Evaluate for malaria.
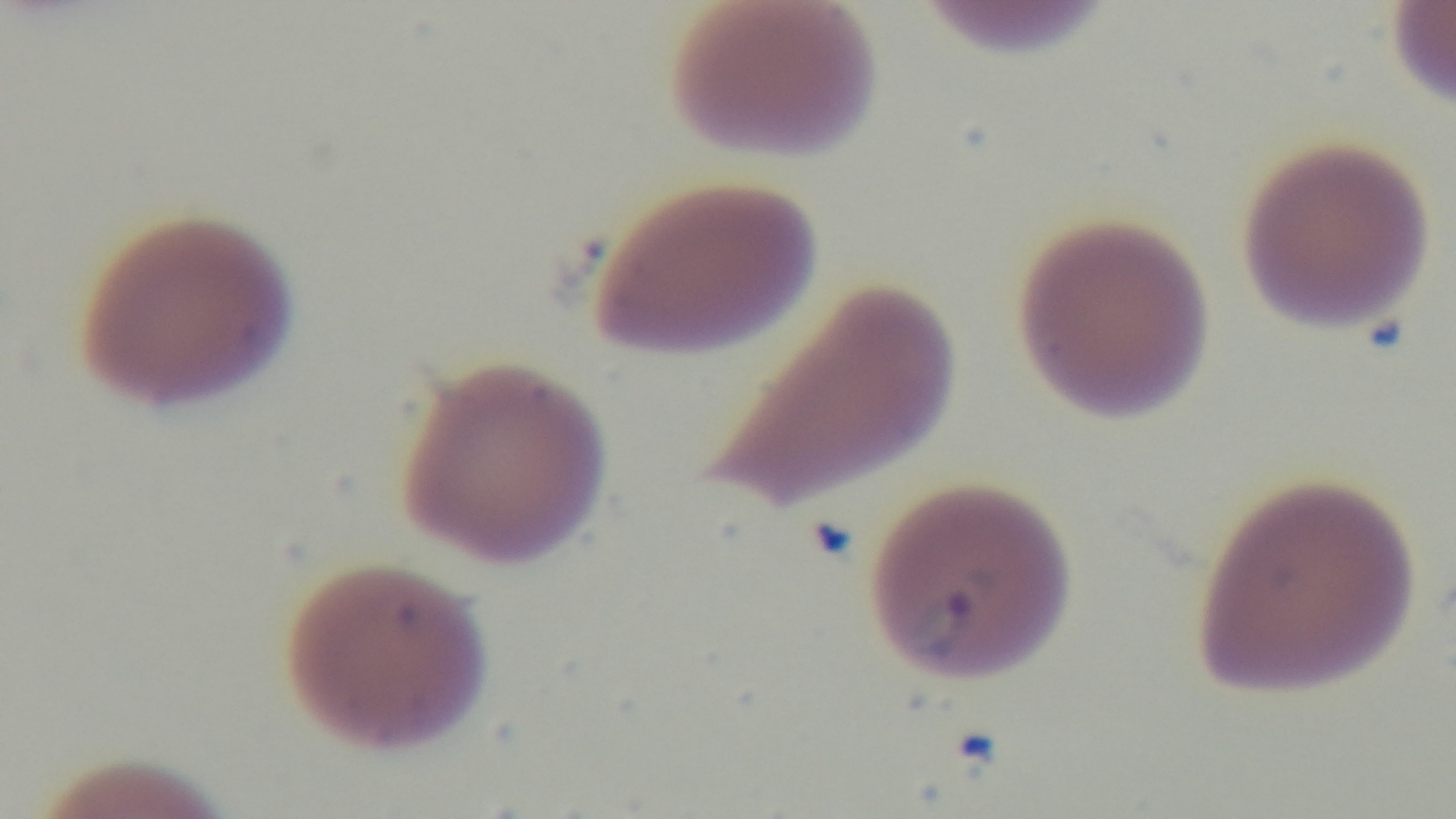
Positive.

Summary:
  - Stain: Giemsa
  - Capture: mounted 4K digital camera
  - Objective: 100x oil immersion
  - Field of view: one from the slide
  - Preparation: thin smear
  - Modality: light microscopy